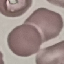
Result: no malaria parasites seen. Thin blood film. Giemsa-stained preparation. Cell patch, automatically extracted from a larger field of view and resized to 64 × 64 pixels. Photographed with a smartphone camera at the microscope eyepiece.